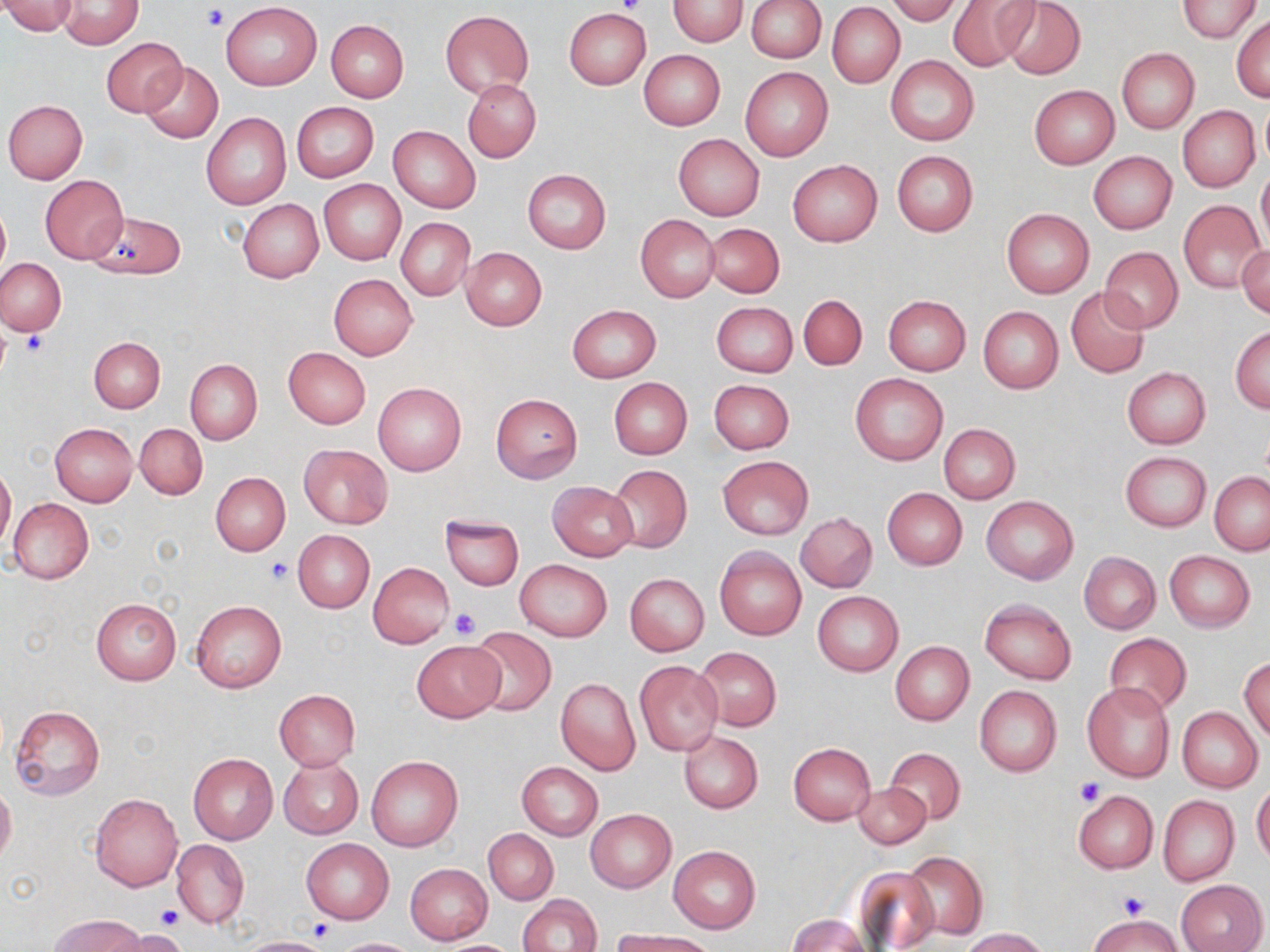

Approximate bounding boxes as (x1,y1)-(x2,y2) corner pairs in pixels. Uninfected red blood cell locations: (669,0)-(748,47), (747,0)-(827,62), (886,0)-(963,24), (947,0)-(1038,72), (997,0)-(1086,80), (1177,0)-(1260,42), (55,1)-(144,49), (0,2)-(80,36), (221,2)-(321,90), (828,2)-(904,88), (440,9)-(533,97), (564,10)-(649,88), (1232,13)-(1270,102), (326,19)-(409,102), (101,36)-(187,117), (1116,48)-(1199,134), (638,50)-(725,129), (885,54)-(979,146), (139,60)-(224,143), (740,67)-(834,161), (463,79)-(541,163), (1029,85)-(1120,169), (3,99)-(89,184), (1258,99)-(1270,171), (292,102)-(379,182), (1178,105)-(1259,192), (201,113)-(291,211), (388,125)-(480,213), (673,133)-(764,220), (891,150)-(978,235), (1088,151)-(1177,233), (787,160)-(883,246), (1256,168)-(1270,251), (522,170)-(611,254), (40,176)-(128,263), (318,180)-(405,263), (238,199)-(324,282), (1179,199)-(1267,294), (0,204)-(9,279), (1003,208)-(1094,297), (85,211)-(186,280), (635,215)-(720,301), (395,217)-(475,300), (704,222)-(785,298), (1236,245)-(1269,321), (1099,246)-(1183,334), (461,248)-(547,329), (0,258)-(67,336), (328,274)-(417,361), (1066,287)-(1150,378), (796,295)-(868,370), (883,295)-(971,376), (712,301)-(797,376), (567,305)-(660,382), (978,306)-(1063,393), (1230,327)-(1270,413), (89,337)-(165,412), (283,346)-(371,428), (185,359)-(262,445), (1121,366)-(1211,448), (850,372)-(947,466), (608,377)-(692,458), (709,380)-(794,454), (372,383)-(466,477), (490,393)-(583,484), (50,423)-(138,506), (134,423)-(207,501), (939,424)-(1019,503), (298,444)-(393,528), (1121,452)-(1211,531), (717,455)-(813,540), (0,463)-(16,553), (607,464)-(692,551), (211,472)-(290,555), (1209,472)-(1270,554), (547,482)-(637,562), (883,488)-(967,570), (981,495)-(1078,583), (8,497)-(94,583), (796,512)-(878,593), (441,514)-(523,590), (293,530)-(375,612), (714,546)-(807,640), (1079,551)-(1161,634), (1165,551)-(1254,632), (514,560)-(612,641), (369,562)-(454,647), (625,574)-(709,656), (814,592)-(902,674), (91,597)-(182,685), (979,598)-(1076,685), (191,600)-(286,692), (466,626)-(557,716), (1103,633)-(1191,715), (412,640)-(507,722), (890,641)-(975,725), (694,646)-(781,731), (1240,657)-(1270,743), (634,661)-(723,756), (556,678)-(641,775), (1082,682)-(1175,781), (975,685)-(1061,776), (274,689)-(361,770), (8,705)-(106,802), (1177,707)-(1262,792), (678,730)-(763,813), (789,742)-(875,824), (885,748)-(965,826), (188,753)-(277,843), (367,755)-(463,852), (277,756)-(363,839), (516,761)-(603,839), (0,781)-(16,867), (1252,781)-(1270,865), (851,783)-(932,850), (1073,789)-(1158,873), (90,793)-(183,892), (1158,795)-(1239,887), (585,809)-(676,892), (483,829)-(558,904), (301,838)-(394,923), (170,839)-(250,929), (668,845)-(761,932), (902,850)-(987,940), (405,863)-(492,944), (855,866)-(942,951), (1176,879)-(1267,952), (518,894)-(602,952), (48,914)-(147,951), (1088,914)-(1185,952), (788,915)-(870,952), (960,927)-(1052,952), (112,929)-(189,952), (609,930)-(717,952), (237,936)-(334,952), (334,937)-(421,951), (432,939)-(523,951). Platelet locations: (616,0)-(646,16), (202,5)-(229,32), (19,330)-(47,356), (265,557)-(294,584), (448,607)-(481,640), (1076,777)-(1105,804), (1118,892)-(1149,919), (157,904)-(183,930). Slide-level diagnosis: no evidence of blood parasites. May-Grünwald-Giemsa stain. Light microscopy. Captured at 1000x magnification. Thin blood film. Single field of view. Image is 1270×952 pixels.